Point out leukocytes.
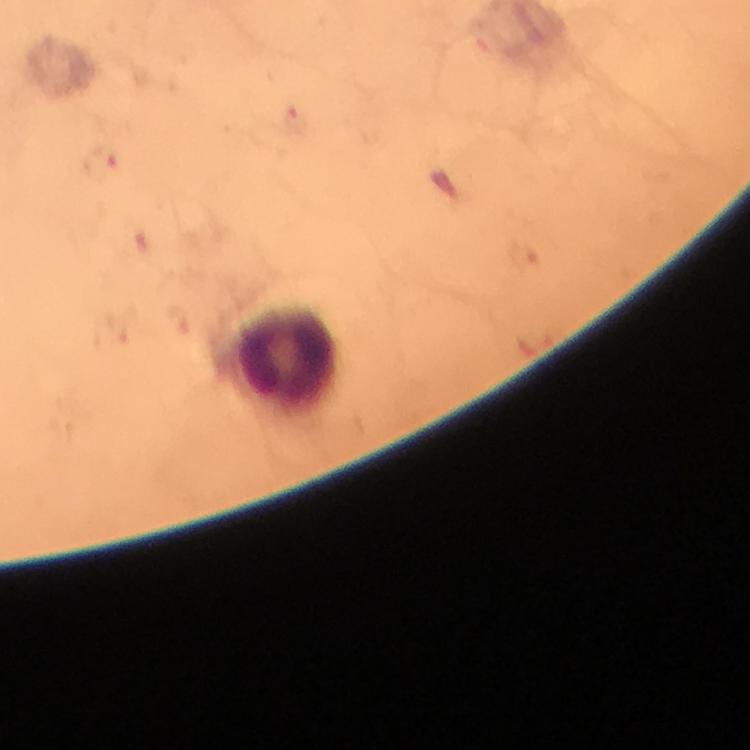
Approximate object centers, in pixels from the top-left corner.
Leukocytes: (x=290, y=358).

Summary:
  - Preparation: thick blood smear
  - Magnification: 100x
  - Capture: smartphone mounted on the microscope
  - Immersion oil: used
  - Stain: Giemsa
  - Image size: 750×750 pixels
  - Context: from a malaria diagnostic workup
  - Cropped from: one field of view
  - Plasmodium parasites: none seen